Point out each Plasmodium parasite.
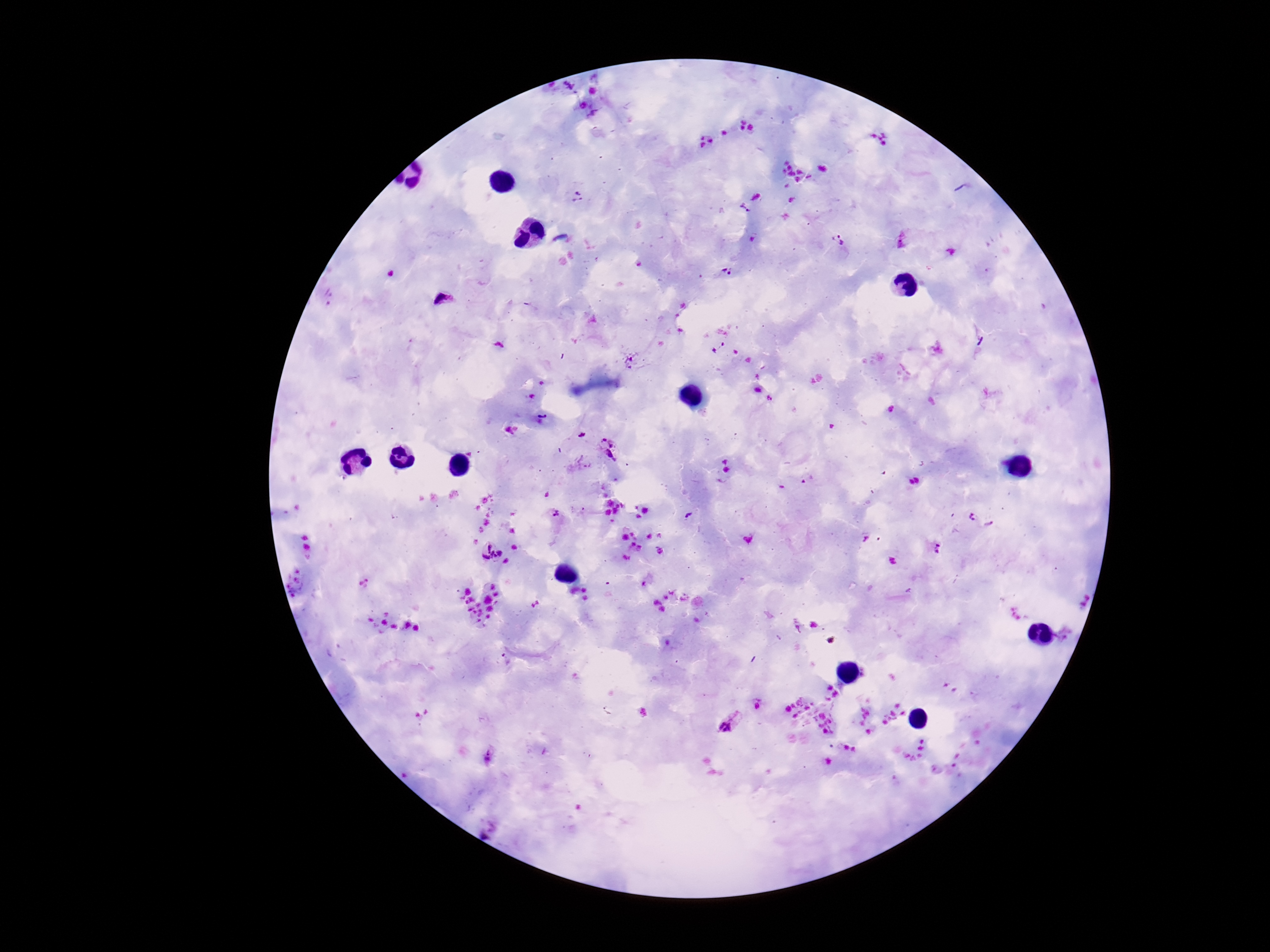
Approximate centers as {x, y} in pixels.
Plasmodium parasites: {592, 91}, {583, 106}, {745, 121}, {752, 128}, {742, 129}, {725, 133}, {701, 138}, {710, 141}, {702, 146}, {578, 196}, {744, 209}, {838, 240}, {725, 272}, {717, 347}, {630, 362}, {757, 390}, {769, 398}, {582, 434}, {609, 449}, {556, 513}, {972, 515}, {989, 524}, {933, 547}, {491, 550}, {730, 721}, {487, 756}.

Summary:
  - Field of view: one from this slide
  - Capture: smartphone camera through the microscope eyepiece
  - Image size: 1270×952 pixels
  - Magnification: 100x
  - Preparation: thick blood smear
  - Patient malaria status: infected
  - Stain: Giemsa